Assess this cell for malaria.
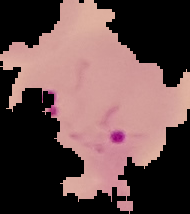
Parasitized.

preparation = thin blood film
image size = 190×214 pixels
image type = segmented cell region on a black background